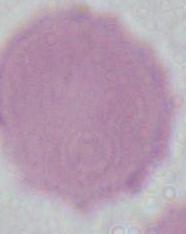

Summary:
  - Magnification: 1000x
  - Modality: photomicrograph
  - Identification: red blood cell